Report the malaria status of this cell.
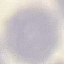

Uninfected.

Summary:
  - Preparation: thin blood smear
  - Stain: Giemsa
  - Image type: automatically extracted cell patch, resized to 64 × 64 pixels
  - Capture: smartphone camera at the microscope eyepiece